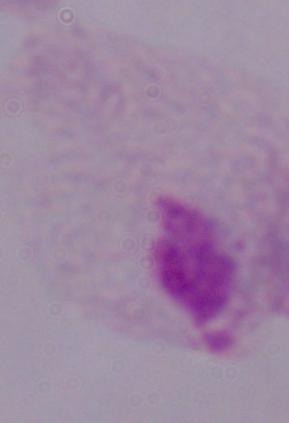

identification = trichomonad
magnification = 1000x
modality = micrograph